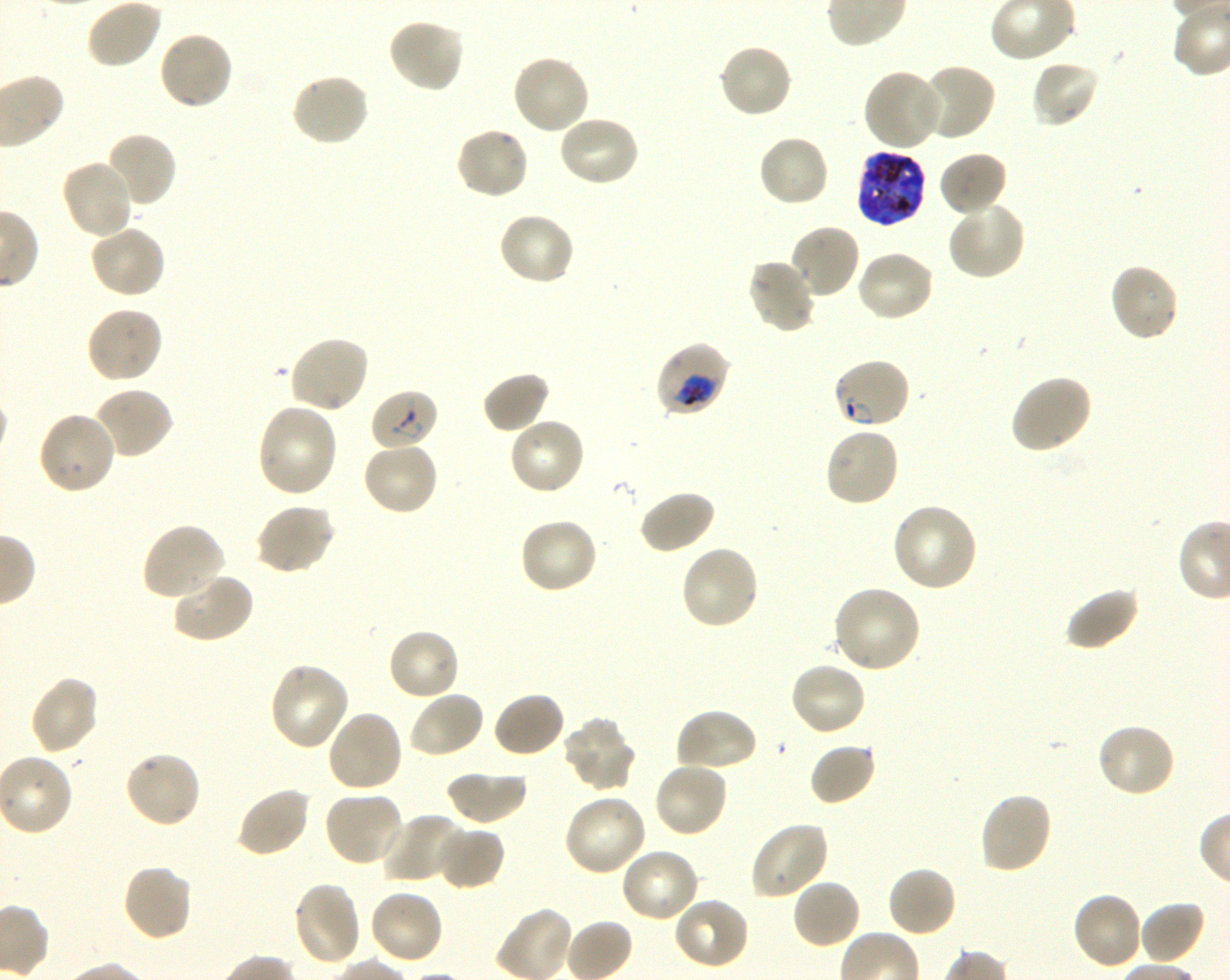 Approximate bounding boxes as {x1, y1, x2, y2} in pixels. Not every red blood cell is marked. A life-cycle stage — or a range of stages, where the recorded stages span more than one — follows each staged infected red blood cell. Locations of red blood cells of indeterminate infection status: {370, 389, 439, 452}. Locations of infected red blood cells: {854, 150, 927, 228} late trophozoite to late schizont; {654, 340, 731, 417} trophozoite; {832, 358, 912, 431} ring. Locations of uninfected red blood cells: {85, 0, 162, 70}, {387, 17, 466, 94}, {157, 30, 234, 111}, {717, 43, 794, 120}, {510, 52, 591, 135}, {1030, 59, 1101, 129}, {919, 63, 997, 143}, {862, 68, 945, 153}, {288, 72, 371, 148}, {556, 114, 640, 189}, {455, 126, 531, 199}, {105, 131, 178, 208}, {757, 134, 830, 209}, {938, 150, 1008, 218}, {59, 158, 135, 240}, {946, 200, 1026, 281}, {497, 211, 576, 287}, {788, 222, 861, 299}, {88, 224, 167, 299}, {855, 250, 935, 324}, {746, 258, 818, 335}, {1108, 262, 1180, 343}, {84, 307, 164, 385}, {287, 334, 370, 415}, {481, 371, 552, 434}, {1008, 373, 1093, 454}, {93, 386, 175, 460}, {255, 401, 340, 498}, {36, 410, 117, 496}, {507, 415, 586, 496}, {823, 425, 901, 508}, {361, 441, 439, 516}, {637, 489, 716, 555}, {891, 502, 980, 593}, {254, 503, 336, 575}, {519, 516, 599, 594}, {140, 522, 226, 602}, {679, 544, 761, 631}, {171, 571, 256, 645}, {831, 585, 922, 675}, {1064, 586, 1141, 652}, {387, 627, 462, 701}, {268, 661, 350, 752}, {789, 662, 867, 737}, {29, 676, 100, 755}, {408, 690, 485, 759}, {492, 691, 567, 759}, {674, 707, 758, 773}, {325, 709, 404, 794}, {563, 718, 637, 793}, {1095, 721, 1177, 798}, {808, 741, 877, 806}, {123, 749, 202, 828}, {653, 760, 729, 839}, {445, 769, 528, 825}, {235, 786, 311, 859}, {323, 790, 406, 867}, {977, 791, 1053, 875}, {562, 793, 648, 878}, {381, 814, 469, 885}, {749, 820, 830, 900}, {435, 824, 505, 890}, {619, 847, 701, 924}, {120, 863, 193, 943}, {886, 866, 958, 939}, {791, 878, 862, 950}, {291, 881, 363, 967}, {368, 888, 445, 966}, {1070, 891, 1144, 971}, {670, 897, 750, 971}, {1138, 901, 1206, 964}. Life-cycle stages observed: ring, trophozoite. Giemsa stain. Image is 1230×980 pixels. Oil immersion, 100x objective (numerical aperture 1.30). Single field of view. Thin blood smear. P. falciparum strain 3D7 maintained in shaking in-vitro culture. Donor blood group O+.